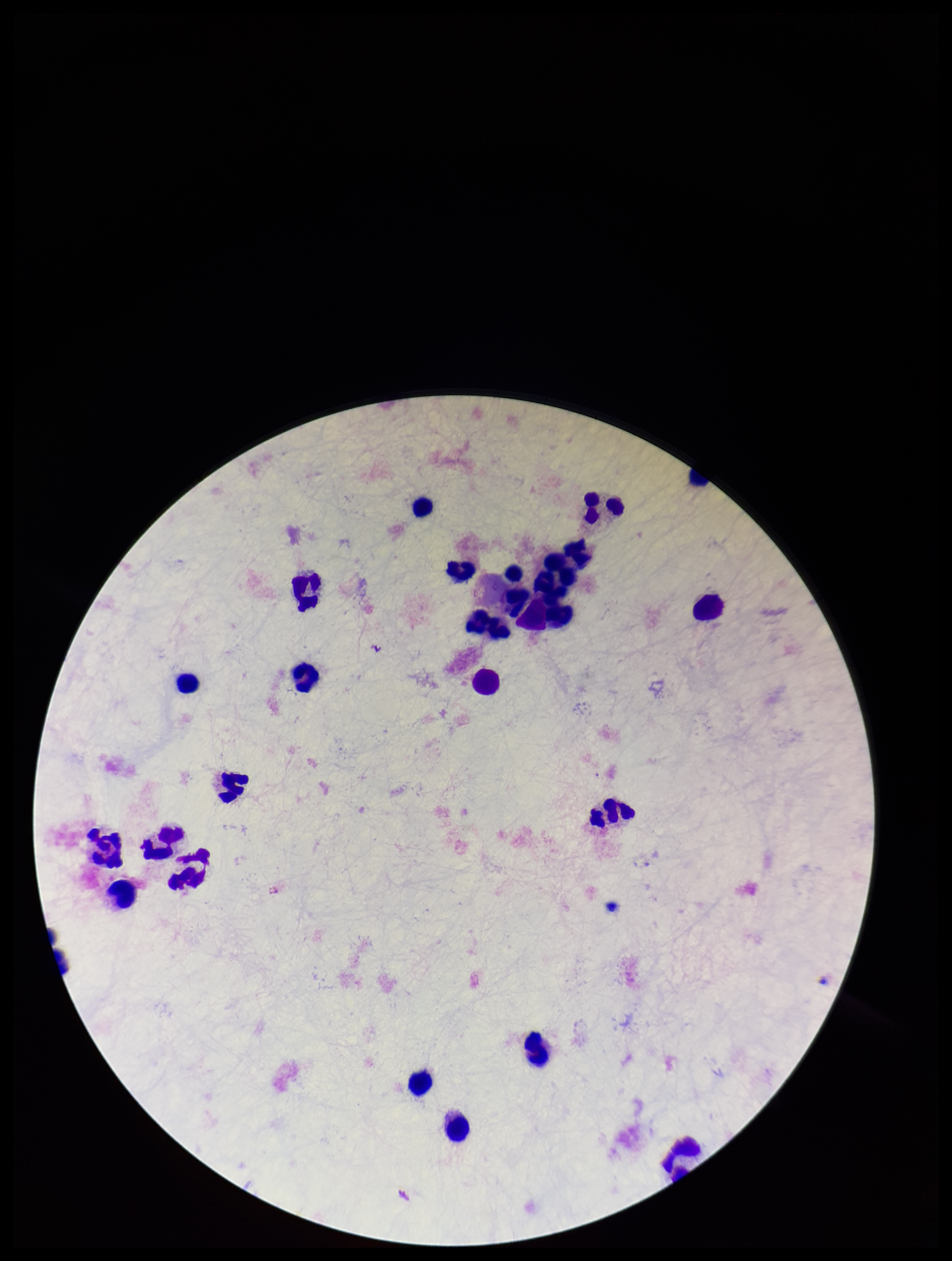
Summary:
  - Stain: Giemsa
  - Plasmodium parasites: none detected
  - Parasite count: 0
  - Preparation: thick blood smear
  - Image size: 952×1261 pixels
  - Leukocyte count: 26
  - Patient malaria status: negative
  - Field of view: single
  - Capture: smartphone photograph through the microscope eyepiece